Locate every Plasmodium parasite.
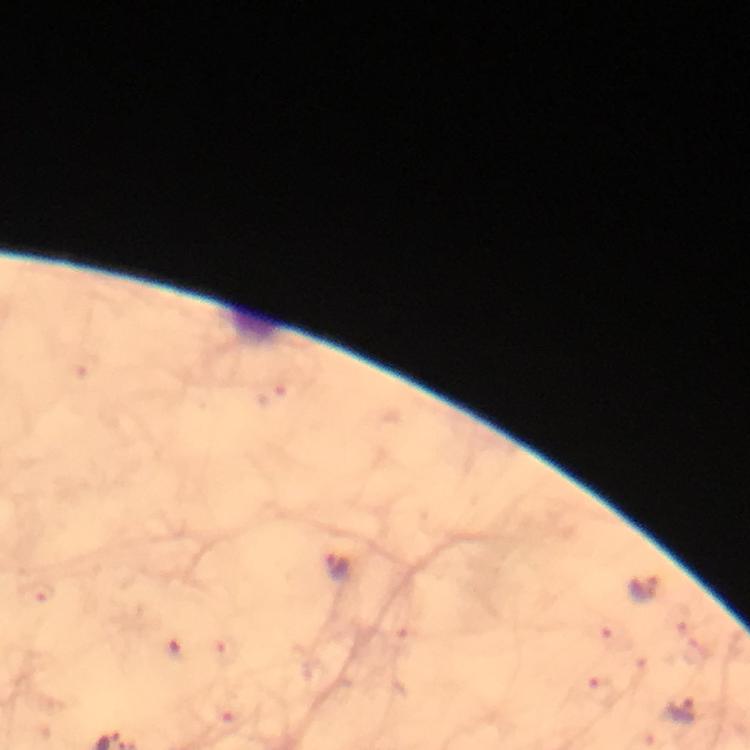
Approximate object centers, in pixels from the top-left corner.
Plasmodium parasites: (x=270, y=397), (x=336, y=566), (x=643, y=590), (x=41, y=592), (x=175, y=647), (x=681, y=710).

Summary:
  - Cropped from: one field of view
  - Context: from a diagnostic examination for malaria
  - Capture: smartphone camera through the microscope
  - Immersion oil: applied
  - Image size: 750×750 pixels
  - Preparation: thick smear
  - Magnification: 100x
  - Stain: Giemsa